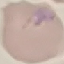
Summary:
  - Malaria status: parasitized
  - Preparation: thin smear
  - Stain: Giemsa
  - Image type: automatically extracted cell patch, resized to 64 × 64 pixels
  - Capture: smartphone camera at the microscope eyepiece